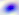
400x magnification. Photomicrograph. Toxoplasma gondii is shown.